Look for Plasmodium parasites.
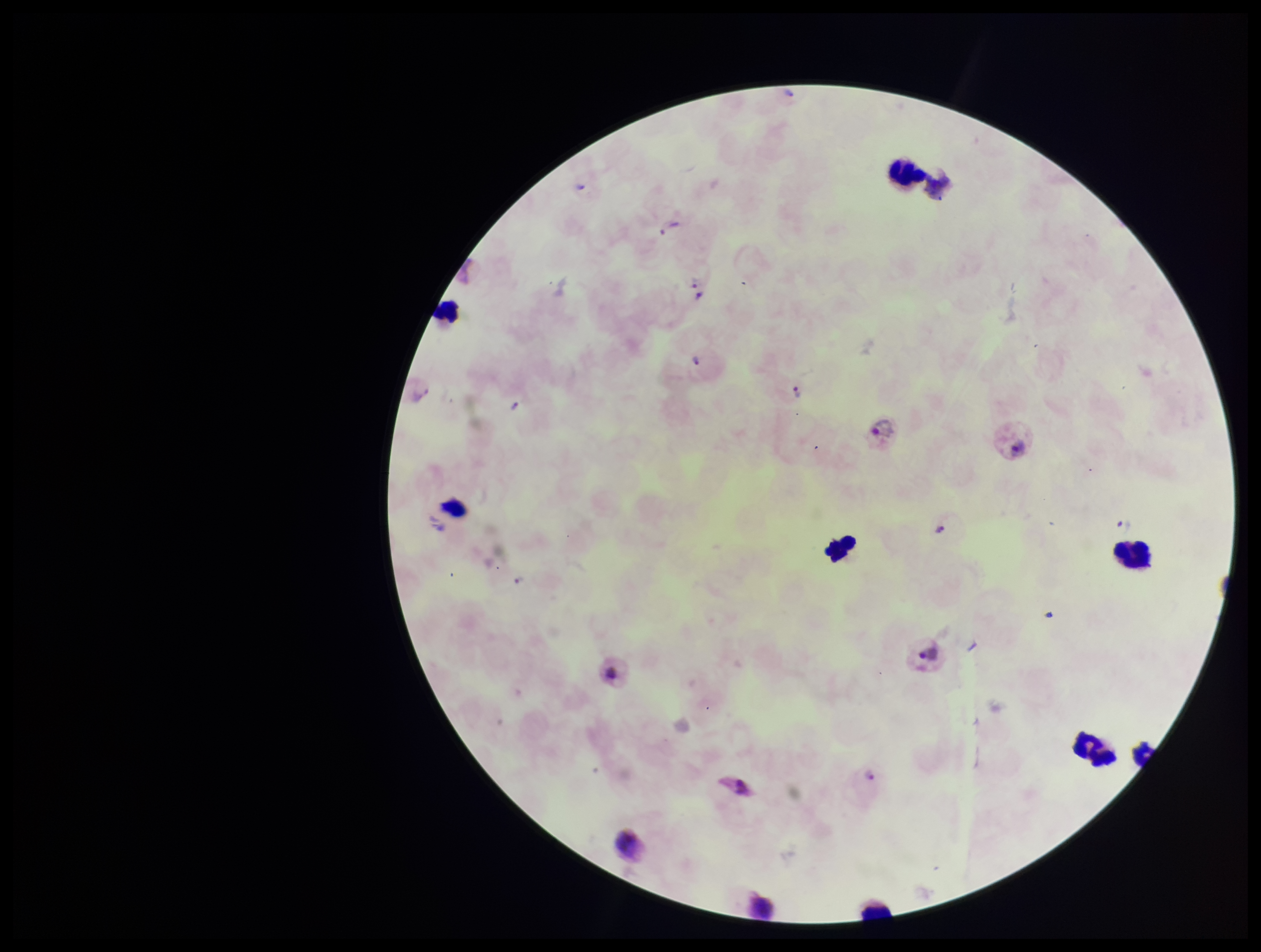
Detected.

image_size: 1261×952 pixels
parasite_count: 9
field_of_view: single
patient_malaria_status: positive
leukocyte_count: 10
species_reported_for_this_patient: Plasmodium vivax
capture: smartphone photograph through the microscope eyepiece
stain: Giemsa
preparation: thick